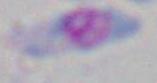 Photomicrograph. 1000x magnification. Toxoplasma gondii is seen.